Assess this cell for malaria.
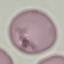

It is uninfected.

Cell patch, automatically extracted from a larger field of view and resized to 64 × 64 pixels. Acquired by smartphone through the microscope eyepiece. Thin blood smear. Giemsa-stained preparation.